Classify this cell by malaria status.
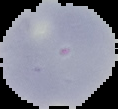
Uninfected.

preparation = thin blood smear
image size = 118×109 pixels
image type = segmented cell region with the area outside set to black